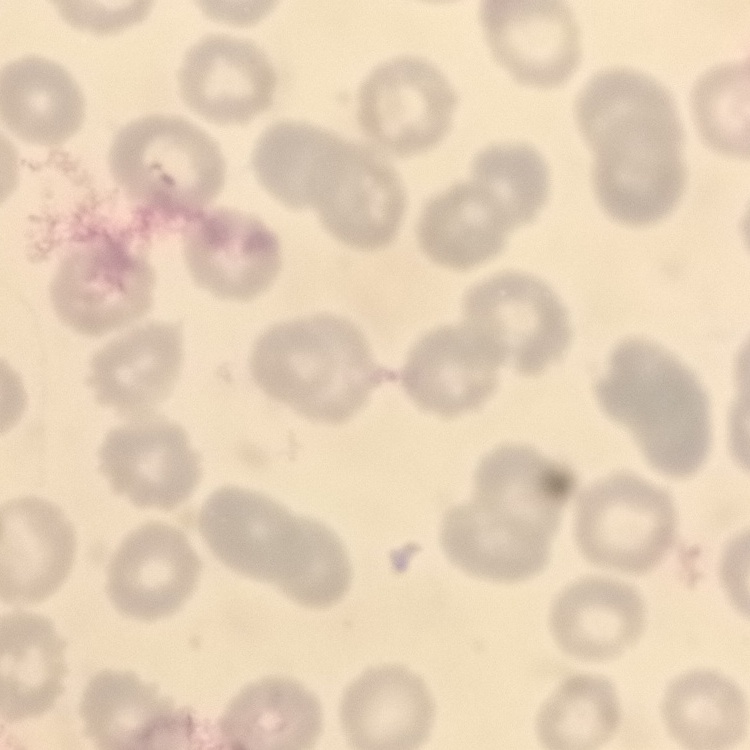

Summary:
  - Red blood cell morphology: no rouleaux formation
  - Stain: Field's or Giemsa
  - Preparation: thin blood film
  - Image type: square crop of a larger photomicrograph